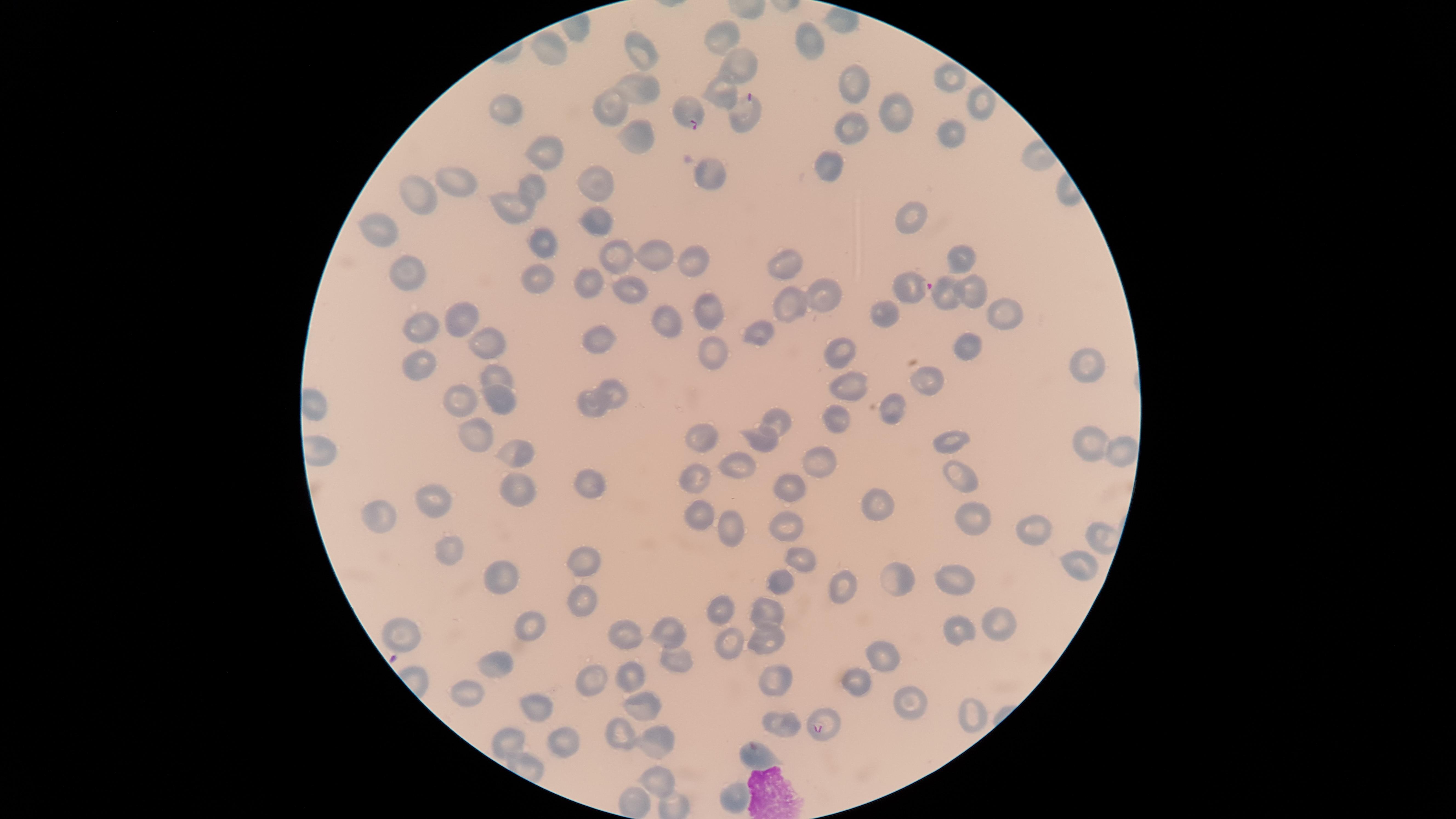

visible region = circular
capture = smartphone photograph through the microscope eyepiece
field of view = single
uninfected red blood cells = approximate marker points as (x, y) in pixels: (723, 31), (810, 44), (549, 48), (638, 48), (739, 61), (854, 76), (946, 76), (722, 91), (635, 92), (983, 102), (602, 106), (501, 112), (893, 113), (855, 128), (636, 131), (953, 136), (549, 148), (831, 167), (710, 173), (458, 182), (596, 183), (530, 194), (418, 197), (513, 206), (602, 215), (908, 219), (373, 227), (541, 238), (653, 253), (615, 255), (691, 258), (959, 259), (781, 263), (408, 273), (542, 281), (585, 282), (631, 290), (976, 290), (824, 294), (947, 295), (709, 304), (783, 305), (878, 311), (1000, 313), (665, 317), (462, 319), (419, 327), (758, 329), (490, 342), (601, 342), (971, 343), (708, 349), (844, 358), (1084, 365), (420, 366), (497, 374), (929, 379), (848, 383), (613, 390), (499, 398), (455, 400), (590, 405), (895, 410), (779, 419), (837, 421), (473, 431), (702, 436), (763, 439), (936, 442), (1086, 444), (512, 446), (1120, 450), (823, 462), (736, 464), (960, 474), (698, 481), (586, 482), (791, 486), (522, 487), (437, 498), (877, 505), (379, 515), (701, 517), (974, 517), (786, 527), (736, 533), (1033, 533), (1098, 535), (452, 554), (587, 560), (806, 560), (1086, 564), (898, 577), (956, 579), (777, 581), (511, 588), (844, 588), (579, 596), (723, 611), (767, 611), (996, 621), (525, 627), (619, 632), (961, 632), (404, 634), (673, 634), (765, 642), (724, 643), (881, 651), (673, 655), (497, 661), (628, 677), (779, 680), (586, 681), (852, 681), (468, 694), (903, 700), (536, 705), (640, 708), (966, 712), (783, 723), (617, 727), (513, 741), (563, 742), (660, 744), (761, 758), (654, 777), (738, 798), (640, 805)
stain = Giemsa
image size = 1456×819 pixels
preparation = thin smear of blood
species = Plasmodium falciparum
parasitized red blood cells = approximate marker points as (x, y) in pixels: (685, 110), (748, 113), (912, 285), (822, 724)
presence = malaria parasites seen